Report the malaria status of this cell.
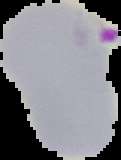

Parasitized.

Image is 121×160 pixels. From a thin blood film. Cell region segmented out of the field of view; the surrounding area is masked to black.